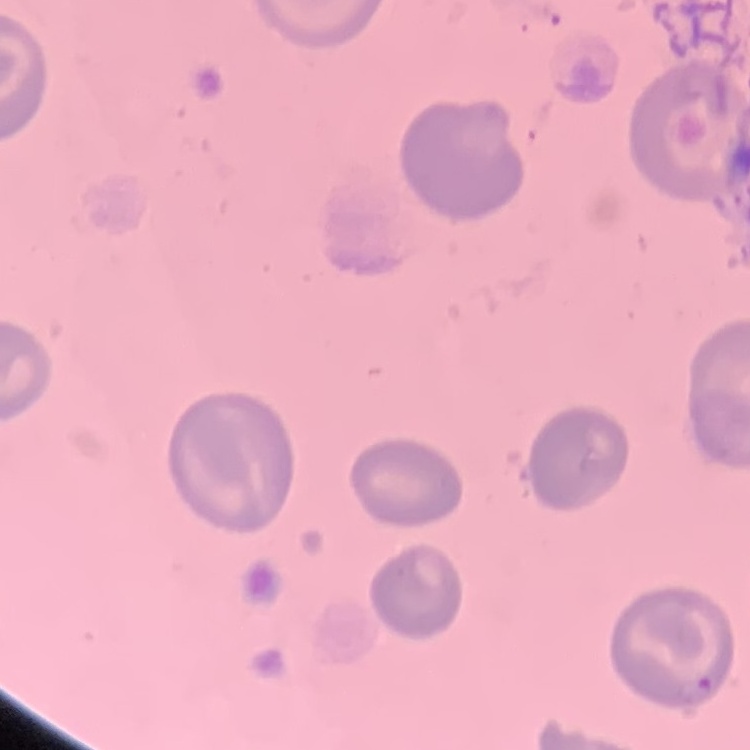
erythrocyte_morphology: no rouleaux formation
preparation: thin blood film
image_type: one tile cut from a larger photomicrograph
stain: Field's or Giemsa